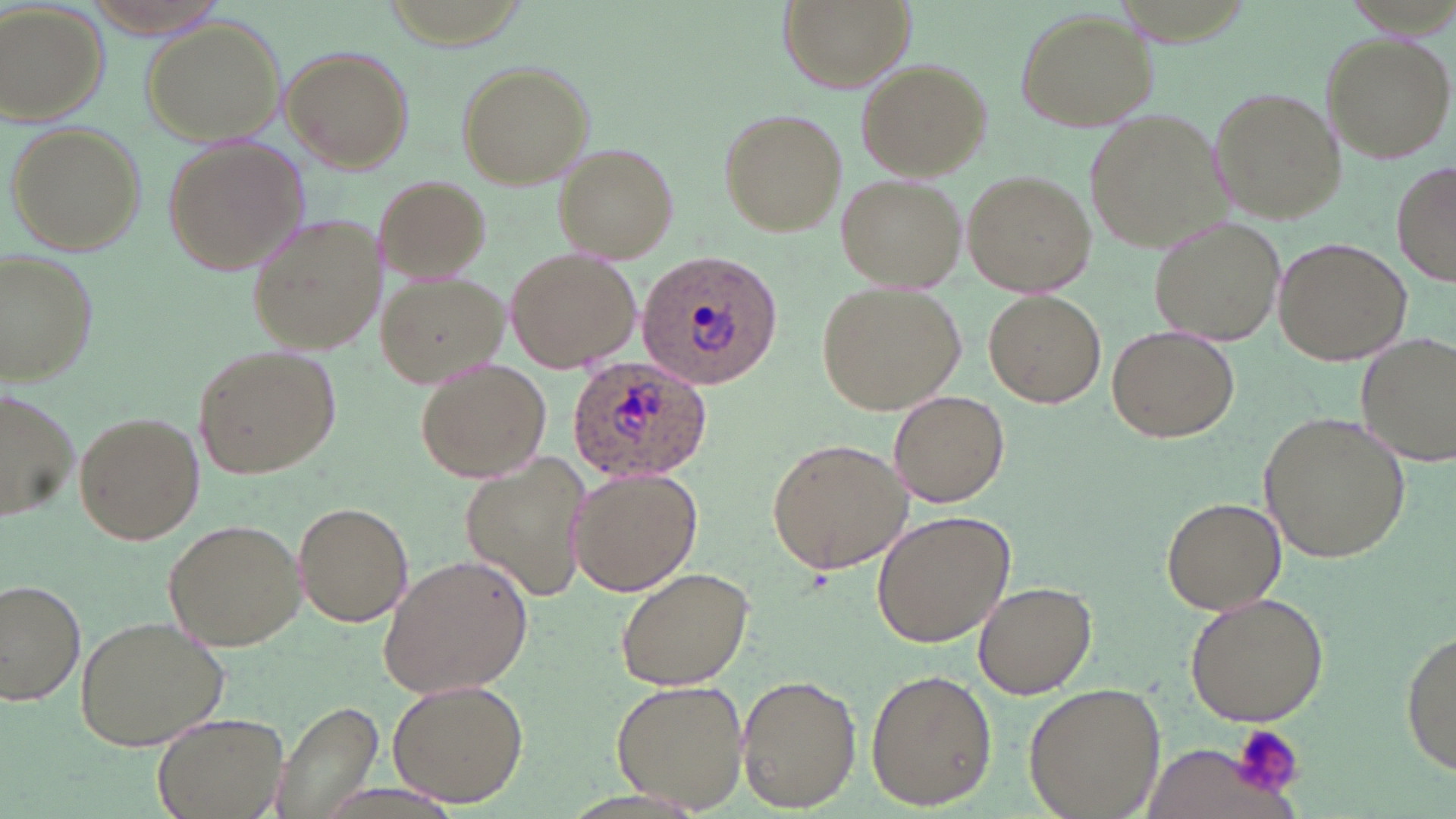 Approximate bounding boxes as named x1/y1/x2/y2 corners in pixels. Plasmodium ovale-infected red blood cell locations: (x1=639, y1=252, x2=784, y2=388), (x1=568, y1=356, x2=712, y2=482). Platelet locations: (x1=1232, y1=722, x2=1304, y2=800). Uninfected red blood cell locations: (x1=775, y1=0, x2=919, y2=96), (x1=0, y1=4, x2=107, y2=125), (x1=1013, y1=9, x2=1159, y2=133), (x1=141, y1=18, x2=286, y2=146), (x1=1321, y1=32, x2=1455, y2=164), (x1=280, y1=44, x2=416, y2=172), (x1=853, y1=58, x2=991, y2=180), (x1=452, y1=59, x2=596, y2=189), (x1=1209, y1=87, x2=1346, y2=222), (x1=1085, y1=107, x2=1230, y2=254), (x1=716, y1=108, x2=845, y2=237), (x1=5, y1=122, x2=146, y2=257), (x1=161, y1=136, x2=307, y2=274), (x1=553, y1=143, x2=679, y2=260), (x1=1392, y1=162, x2=1455, y2=288), (x1=964, y1=170, x2=1098, y2=295), (x1=835, y1=173, x2=966, y2=292), (x1=375, y1=175, x2=492, y2=282), (x1=249, y1=213, x2=384, y2=355), (x1=1152, y1=219, x2=1284, y2=346), (x1=1274, y1=238, x2=1411, y2=367), (x1=0, y1=246, x2=99, y2=385), (x1=507, y1=249, x2=638, y2=372), (x1=375, y1=272, x2=509, y2=389), (x1=817, y1=281, x2=965, y2=413), (x1=984, y1=290, x2=1105, y2=406), (x1=1108, y1=326, x2=1240, y2=442), (x1=1355, y1=332, x2=1456, y2=466), (x1=194, y1=344, x2=339, y2=479), (x1=414, y1=356, x2=551, y2=483), (x1=0, y1=390, x2=79, y2=522), (x1=888, y1=392, x2=1013, y2=507), (x1=72, y1=410, x2=204, y2=545), (x1=1261, y1=412, x2=1413, y2=564), (x1=767, y1=439, x2=912, y2=576), (x1=457, y1=456, x2=592, y2=602), (x1=567, y1=466, x2=702, y2=598), (x1=1162, y1=497, x2=1286, y2=614), (x1=291, y1=502, x2=415, y2=626), (x1=873, y1=511, x2=1014, y2=648), (x1=161, y1=518, x2=304, y2=650), (x1=377, y1=553, x2=532, y2=699), (x1=614, y1=565, x2=756, y2=690), (x1=0, y1=578, x2=87, y2=706), (x1=974, y1=579, x2=1095, y2=697), (x1=1182, y1=591, x2=1331, y2=727), (x1=73, y1=615, x2=229, y2=752), (x1=1400, y1=629, x2=1456, y2=775), (x1=866, y1=668, x2=997, y2=810), (x1=736, y1=673, x2=858, y2=812), (x1=388, y1=678, x2=529, y2=807), (x1=610, y1=679, x2=749, y2=811), (x1=1023, y1=681, x2=1167, y2=818), (x1=265, y1=699, x2=384, y2=819), (x1=151, y1=709, x2=291, y2=819), (x1=1135, y1=741, x2=1298, y2=819). Slide-level diagnosis: Plasmodium ovale. One field of a larger specimen. Image is 1456×819 pixels. Optical microscopy. Thin blood film. May-Grünwald-Giemsa-stained preparation. 1000x magnification.